Locate every blood parasite and identify its species.
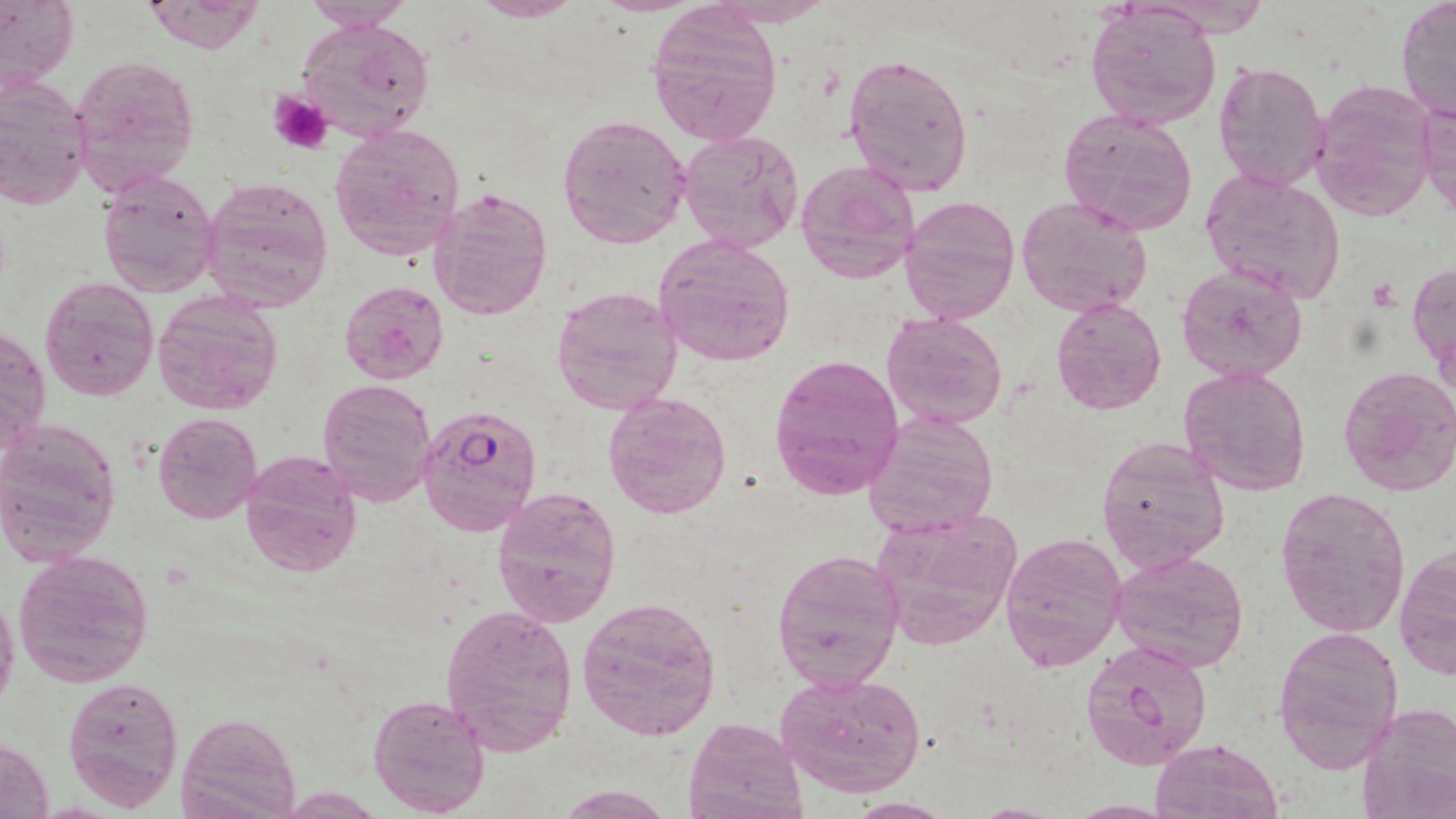

Approximate bounding boxes as [x1, y1, x2, y2] in pixels.
Plasmodium falciparum-infected red blood cells: [417, 405, 543, 537].
No Plasmodium ovale, Plasmodium malariae, Plasmodium vivax, Babesia divergens, or Trypanosoma brucei observed.

Summary:
  - Platelet locations: [268, 91, 334, 156]
  - Uninfected red blood cell locations: [0, 0, 77, 99], [141, 0, 266, 54], [464, 0, 589, 21], [707, 0, 840, 26], [300, 1, 415, 32], [1396, 1, 1456, 121], [1084, 5, 1222, 130], [648, 8, 781, 148], [299, 18, 436, 142], [842, 51, 974, 199], [66, 53, 201, 196], [1212, 59, 1329, 192], [0, 76, 94, 209], [1310, 78, 1439, 219], [1419, 95, 1456, 221], [1057, 106, 1199, 235], [557, 113, 691, 250], [328, 122, 465, 262], [677, 128, 804, 253], [795, 157, 923, 285], [97, 169, 221, 296], [1200, 169, 1347, 307], [200, 175, 335, 313], [428, 185, 554, 322], [898, 193, 1020, 325], [1016, 195, 1154, 316], [652, 232, 797, 368], [1409, 260, 1455, 376], [1176, 265, 1308, 383], [39, 276, 159, 401], [340, 281, 448, 382], [550, 283, 682, 417], [152, 291, 284, 415], [1051, 298, 1167, 416], [882, 311, 1009, 430], [0, 321, 51, 460], [769, 352, 906, 499], [1337, 364, 1456, 499], [1178, 365, 1312, 498], [316, 378, 437, 507], [602, 389, 733, 520], [861, 409, 1001, 538], [153, 413, 262, 524], [0, 419, 121, 565], [1096, 436, 1231, 573], [239, 449, 363, 577], [491, 486, 622, 627], [1272, 488, 1411, 639], [868, 506, 1025, 652], [1000, 531, 1127, 670], [1394, 544, 1455, 680], [772, 547, 905, 695], [14, 549, 155, 689], [1110, 550, 1249, 672], [0, 588, 20, 716], [577, 596, 721, 741], [438, 603, 579, 756], [1272, 625, 1404, 773], [1080, 638, 1214, 771], [774, 670, 927, 800], [63, 675, 184, 810], [368, 690, 491, 816], [1358, 702, 1456, 818], [178, 711, 300, 819], [684, 715, 806, 819], [0, 737, 54, 818], [1150, 738, 1283, 818], [554, 785, 675, 818], [844, 800, 956, 819], [1065, 801, 1177, 818]
  - Slide-level diagnosis: Plasmodium falciparum
  - Magnification: 1000x
  - Image size: 1456×819 pixels
  - Field of view: single
  - Modality: light microscopy
  - Preparation: thin blood film
  - Stain: May-Grünwald-Giemsa